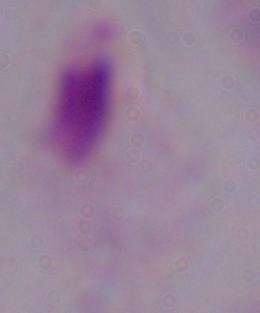

Summary:
  - Magnification: 1000x
  - Modality: micrograph
  - Identification: trichomonad